Assess the morphology of the red blood cells.
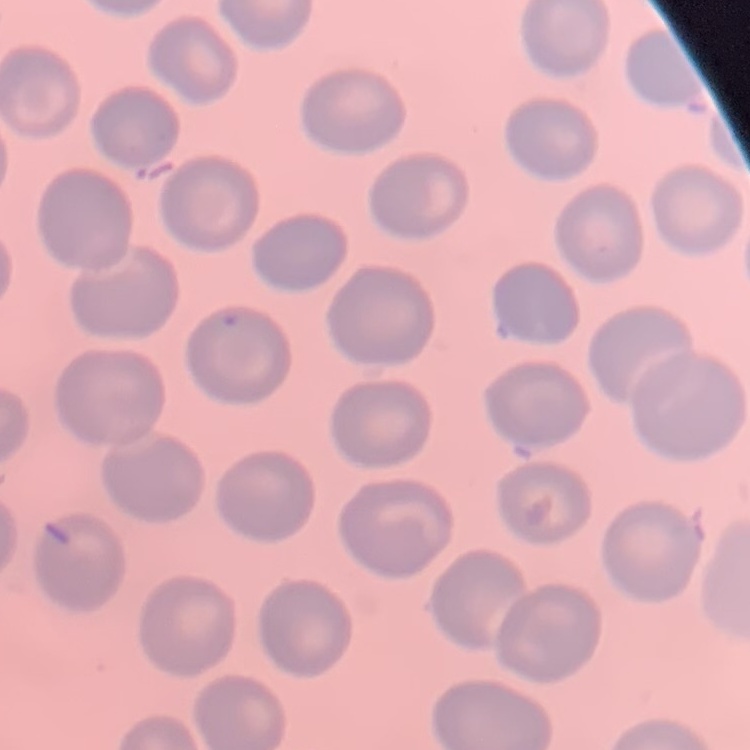
They show no rouleaux formation.

Thin peripheral smear. Stained with either Field's or Giemsa. One tile cut from a larger photomicrograph.